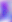
{
  "modality": "micrograph",
  "identification": "Toxoplasma gondii",
  "magnification": "400x"
}